Report the malaria status of this cell.
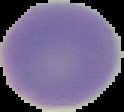

It is uninfected.

Summary:
  - Preparation: thin blood film
  - Image size: 124×112 pixels
  - Image type: cell region segmented out of the field of view; surrounding area masked to black